Assess the morphology of the erythrocytes.
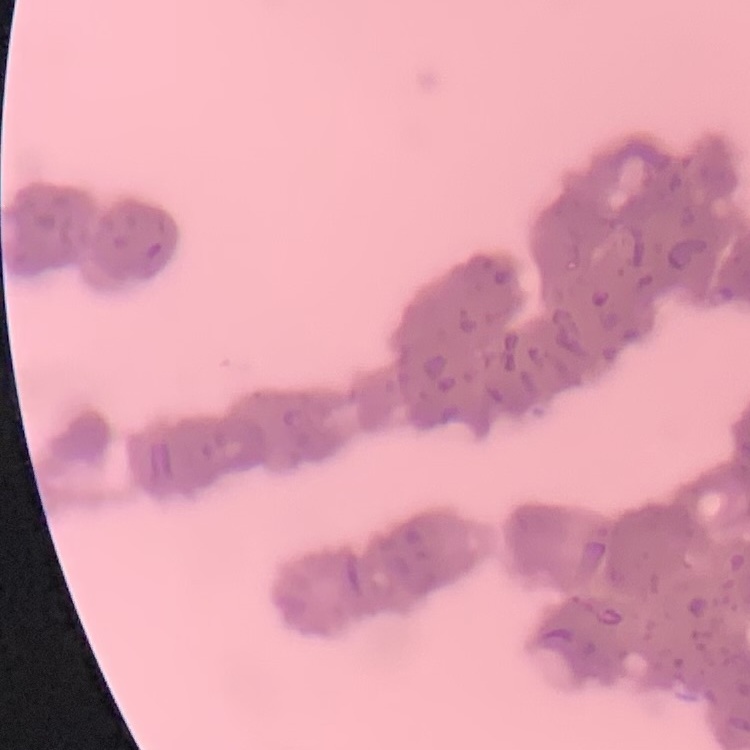

They show rouleaux formation.

Thin blood film. Stained with either Field's or Giemsa. Square crop of a larger photomicrograph.